Evaluate for Plasmodium parasites.
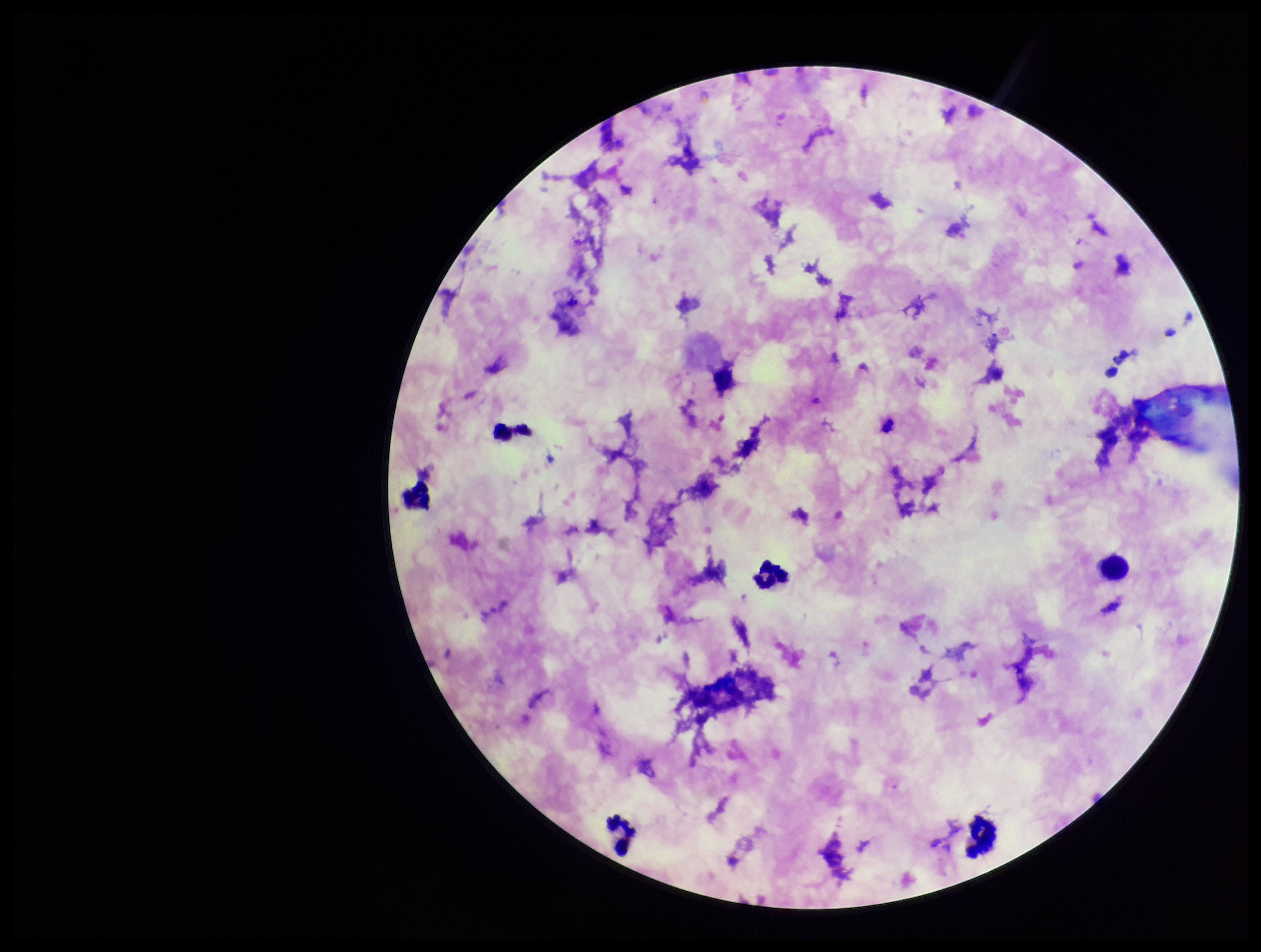

None identified.

{
  "capture": "smartphone photograph through the microscope eyepiece",
  "patient_malaria_status": "positive",
  "preparation": "thick blood smear",
  "parasite_count": 0,
  "species_reported_for_this_patient": "Plasmodium falciparum",
  "field_of_view": "single",
  "leukocyte_count": 7,
  "stain": "Giemsa",
  "image_size": "1261×952 pixels"
}